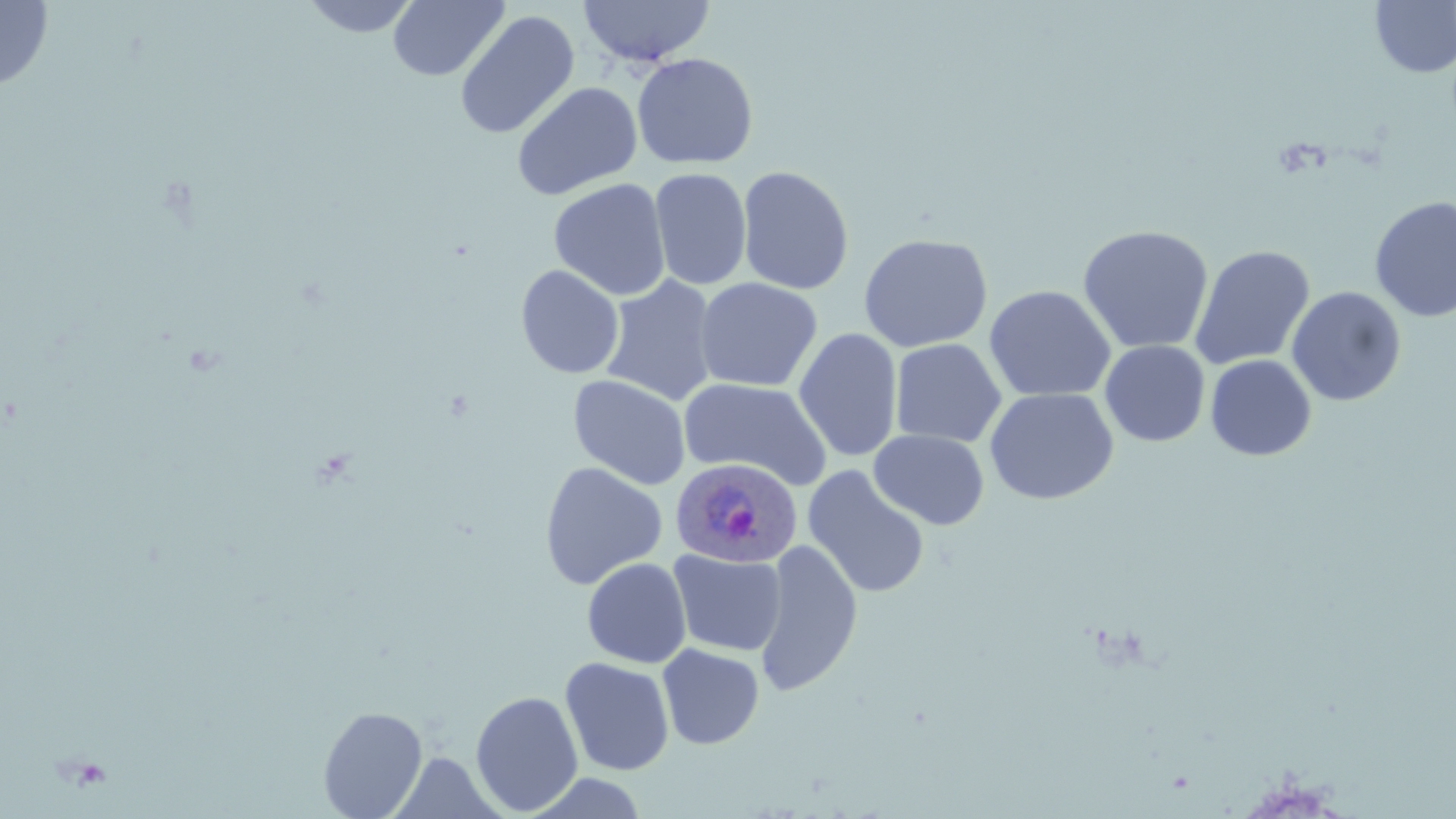
slide-level diagnosis = Plasmodium ovale
preparation = thin blood smear
stain = May-Grünwald-Giemsa
uninfected red blood cell locations = approximate bounding boxes as named x1/y1/x2/y2 corners in pixels: (x1=300, y1=0, x2=422, y2=38), (x1=388, y1=0, x2=509, y2=82), (x1=578, y1=0, x2=715, y2=67), (x1=1370, y1=0, x2=1456, y2=78), (x1=0, y1=1, x2=54, y2=92), (x1=454, y1=10, x2=579, y2=140), (x1=632, y1=52, x2=758, y2=170), (x1=511, y1=81, x2=643, y2=201), (x1=737, y1=165, x2=854, y2=295), (x1=649, y1=168, x2=752, y2=290), (x1=548, y1=178, x2=671, y2=301), (x1=1370, y1=195, x2=1456, y2=322), (x1=1077, y1=224, x2=1214, y2=355), (x1=858, y1=233, x2=993, y2=353), (x1=1190, y1=244, x2=1315, y2=371), (x1=515, y1=264, x2=624, y2=379), (x1=600, y1=275, x2=719, y2=407), (x1=694, y1=277, x2=822, y2=393), (x1=983, y1=285, x2=1117, y2=403), (x1=1286, y1=286, x2=1406, y2=406), (x1=793, y1=328, x2=903, y2=463), (x1=890, y1=338, x2=1007, y2=448), (x1=1100, y1=340, x2=1210, y2=447), (x1=1205, y1=354, x2=1316, y2=461), (x1=568, y1=374, x2=691, y2=490), (x1=679, y1=377, x2=833, y2=491), (x1=984, y1=387, x2=1119, y2=505), (x1=869, y1=430, x2=989, y2=530), (x1=539, y1=461, x2=668, y2=590), (x1=803, y1=466, x2=930, y2=598), (x1=754, y1=538, x2=863, y2=697), (x1=668, y1=549, x2=787, y2=656), (x1=582, y1=557, x2=692, y2=668), (x1=657, y1=644, x2=765, y2=749), (x1=560, y1=657, x2=675, y2=776), (x1=470, y1=690, x2=584, y2=816), (x1=318, y1=705, x2=428, y2=818), (x1=391, y1=753, x2=501, y2=817)
magnification = 1000x
Plasmodium ovale-infected red blood cell locations = approximate bounding boxes as named x1/y1/x2/y2 corners in pixels: (x1=670, y1=457, x2=802, y2=568)
image size = 1456×819 pixels
modality = optical microscopy
field of view = one of a larger specimen